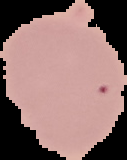
Image is 127×160 pixels. From a thin blood smear. Malaria status: uninfected. The area outside the segmented cell region is set to black.